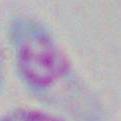
{
  "magnification": "1000x",
  "identification": "Toxoplasma gondii",
  "modality": "micrograph"
}